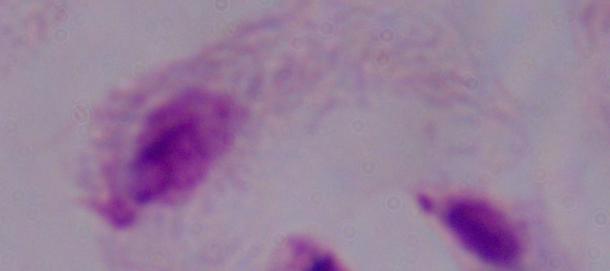

Summary:
  - Magnification: 1000x
  - Modality: photomicrograph
  - Identification: trichomonad